Locate every Plasmodium parasite.
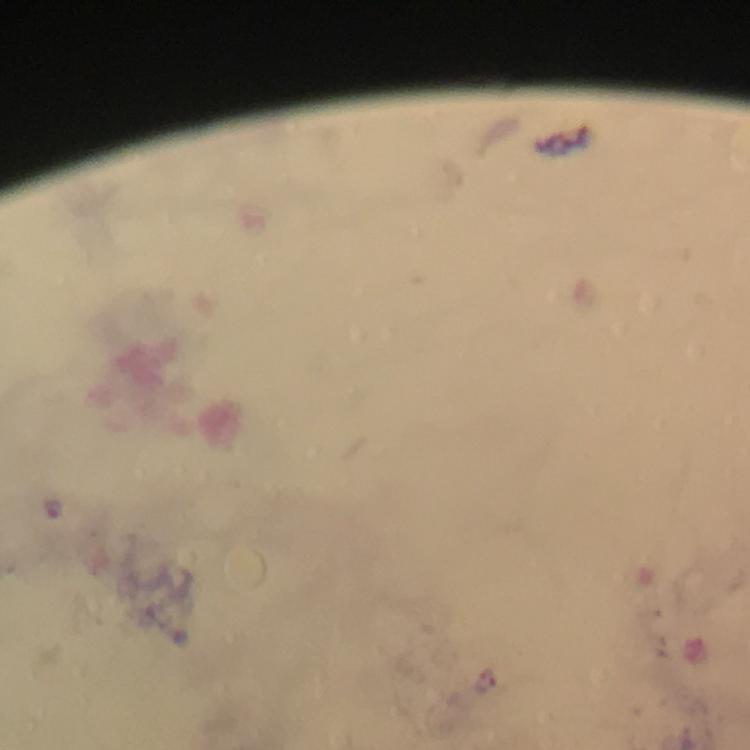
Approximate centers as [x, y] in pixels.
Plasmodium parasites: [52, 507].

Thick blood smear. 100x magnification. From a malaria diagnostic workup. Giemsa-stained preparation. Cropped region of a single field of view. Immersion oil applied. Image is 750×750 pixels. Photographed through the microscope with a smartphone camera.